Name the parasite shown.
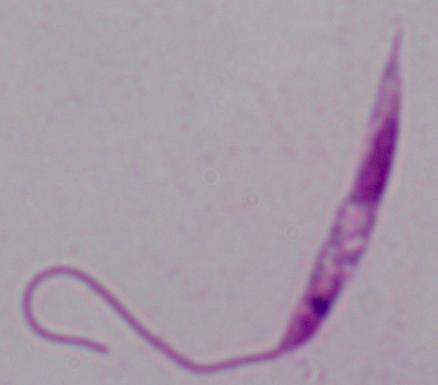
This is Leishmania.

Micrograph. 1000x magnification.